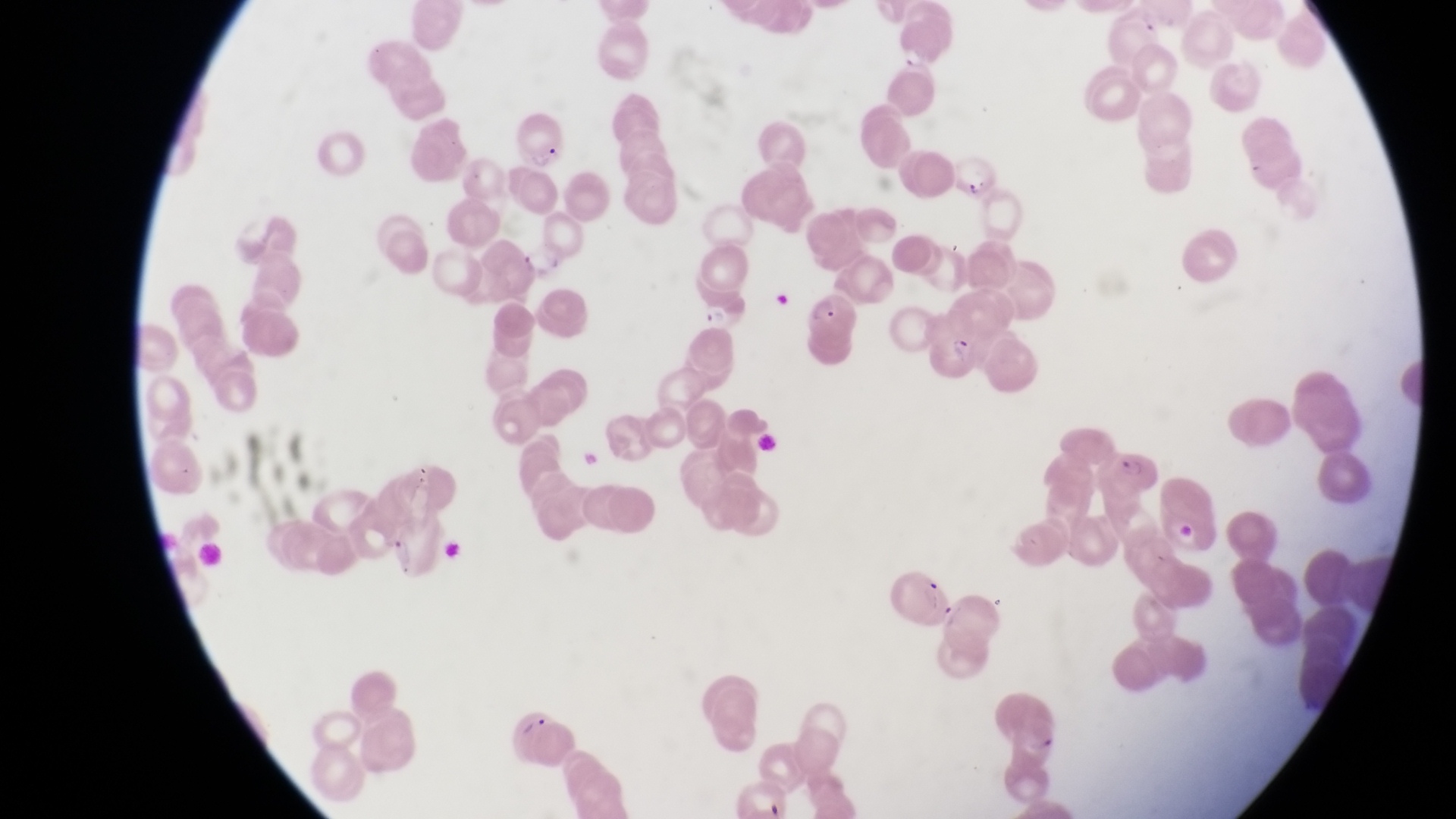
Approximate bounding boxes as left top right bottom in pixels.
Summary:
  - Parasitised red blood cell locations: 941 145 993 200; 701 287 748 334; 809 291 859 344; 930 310 983 376; 1100 442 1163 500
  - Artifact (platelet-like body, stain precipitate, or debris) locations: 436 535 468 569; 519 713 549 742
  - Field of view: single
  - Preparation: thin blood film
  - Image size: 1456×819 pixels
  - Capture: smartphone photograph through the eyepiece of an Olympus CX-23 microscope
  - Country: Uganda
  - Magnification: 1000x